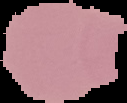
preparation = thin blood film
image type = segmented cell region with the area outside set to black
malaria status = uninfected
image size = 127×103 pixels